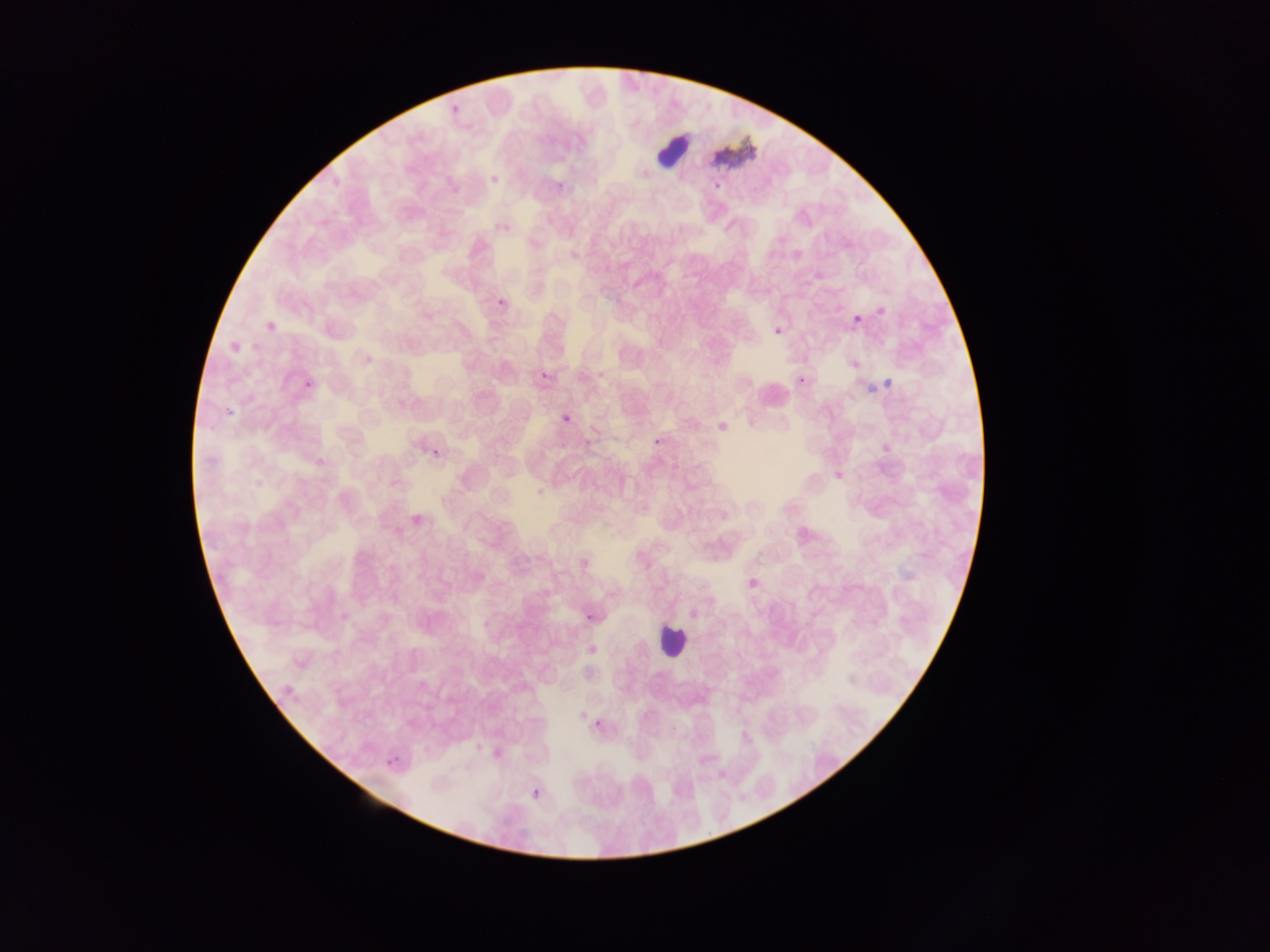

artifact (stain precipitate or debris) locations = approximate bounding boxes as (left, top, right, bottom) in pixels: (712, 132, 754, 168)
country = Ghana
leukocyte locations = approximate bounding boxes as (left, top, right, bottom) in pixels: (656, 130, 687, 166), (657, 621, 687, 659)
field of view = single
image size = 1270×952 pixels
preparation = thin blood film
Plasmodium parasite locations = approximate bounding boxes as (left, top, right, bottom) in pixels: (450, 104, 461, 113), (489, 172, 502, 186), (557, 182, 564, 190), (713, 183, 722, 192), (494, 223, 502, 231), (496, 299, 504, 309), (854, 315, 863, 323), (774, 326, 782, 335), (543, 370, 549, 379), (304, 381, 312, 387), (228, 407, 233, 415), (562, 414, 570, 422), (431, 448, 440, 457), (584, 614, 595, 620), (594, 718, 599, 727), (533, 788, 541, 794) | approximate (x, y) pixel centers of objects too small to bound: (508, 228), (801, 379), (657, 442), (398, 758), (389, 764)
capture = mobile-phone photograph through a microscope